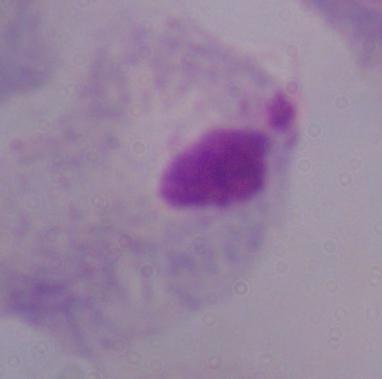
magnification = 1000x
modality = micrograph
identification = trichomonad